Identify the parasite.
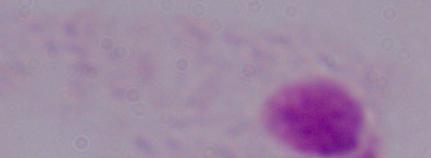
A trichomonad.

magnification = 1000x
modality = photomicrograph